Identify the parasite.
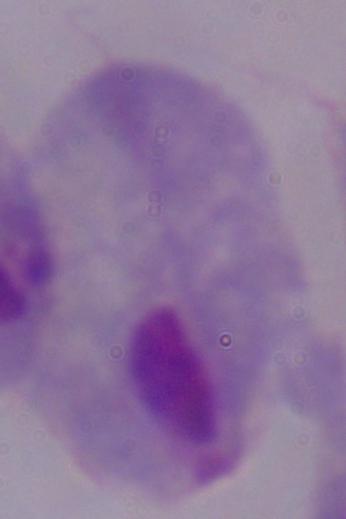
A trichomonad.

Summary:
  - Modality: micrograph
  - Magnification: 1000x